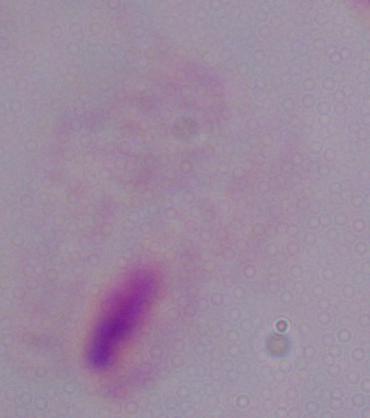 Micrograph. A trichomonad is shown. 1000x magnification.